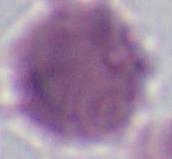

modality: micrograph
identification: erythrocyte
magnification: 1000x